State the preparation type.
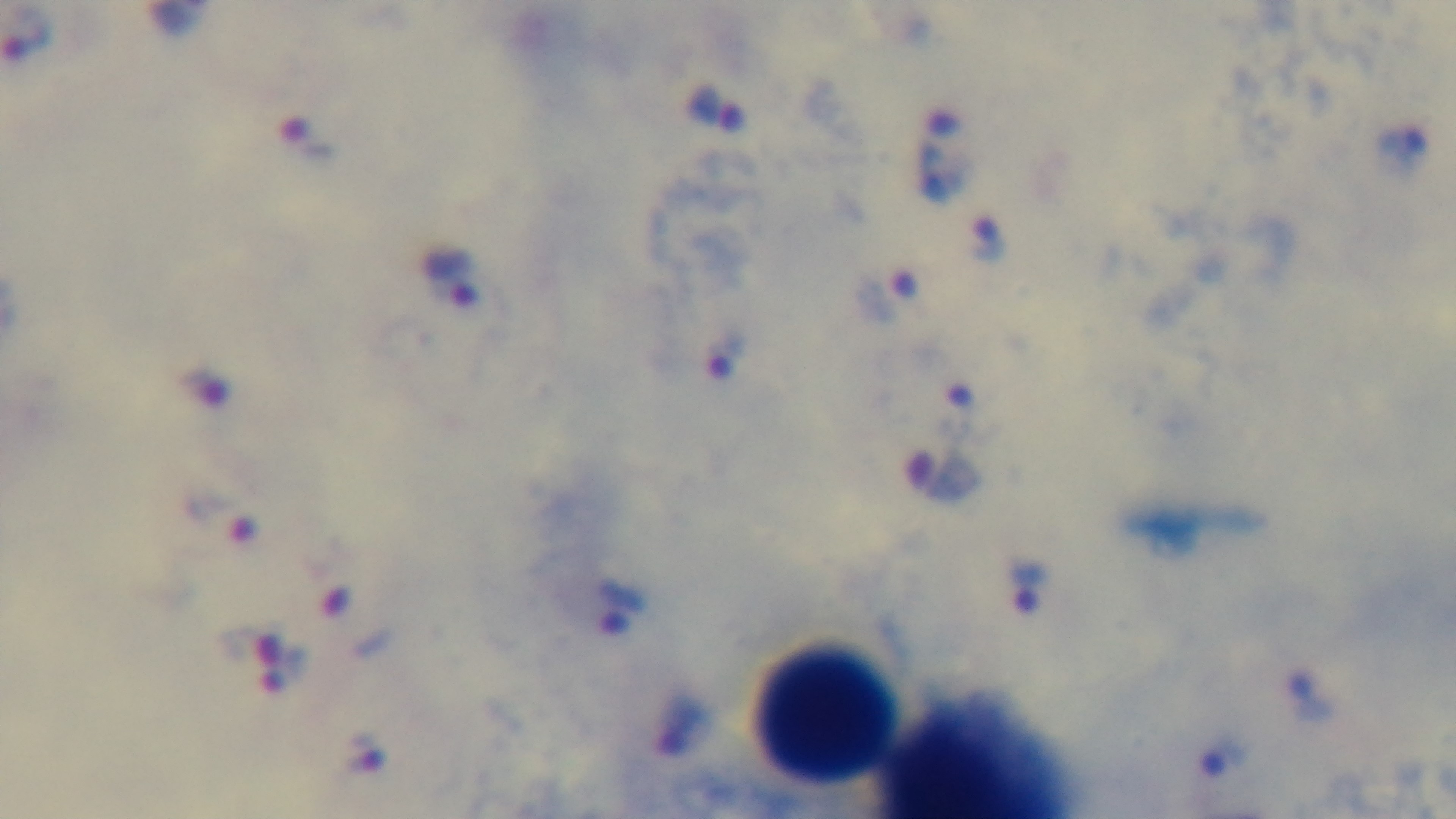
A thick smear.

Light microscopy. Captured with a mounted 4K digital camera. Giemsa stain. Malaria status: infected. Oil-immersion objective, 100x. Single field of view.